Classify this cell by malaria status.
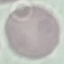
Uninfected.

Summary:
  - Preparation: thin blood smear
  - Capture: smartphone through the microscope eyepiece
  - Stain: Giemsa
  - Image type: cell patch, automatically extracted from a larger field of view and resized to 64 × 64 pixels